Classify this cell by malaria status.
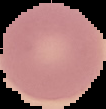
Uninfected.

Summary:
  - Image size: 106×109 pixels
  - Image type: segmented cell region with the area outside set to black
  - Preparation: thin blood smear